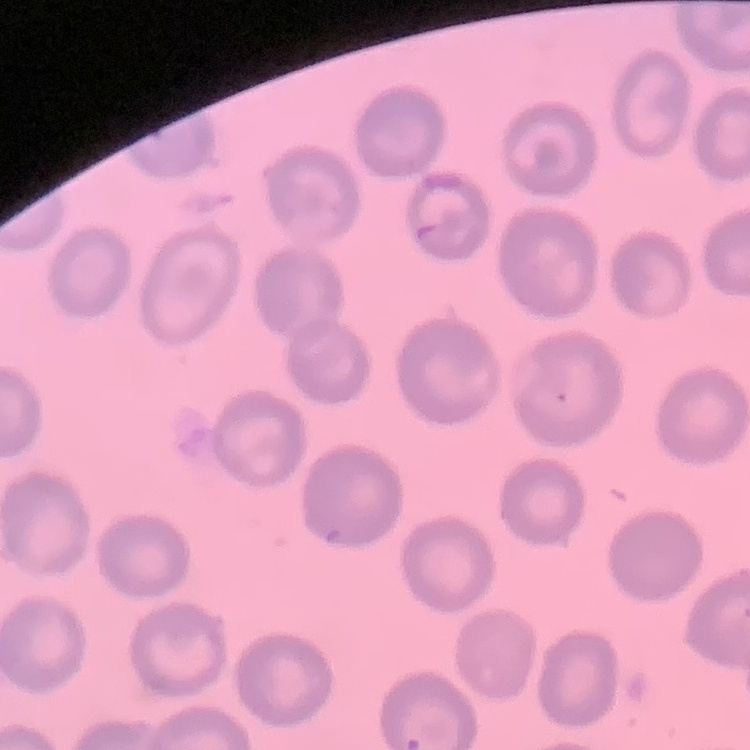

Summary:
  - Red blood cell morphology: no rouleaux formation
  - Stain: Field's or Giemsa
  - Preparation: thin blood smear
  - Image type: square crop of a larger photomicrograph